Assess this cell for malaria.
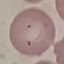
Parasitized.

stain: Giemsa
image_type: automatically extracted cell patch, resized to 64 × 64 pixels
preparation: thin smear
capture: smartphone through the microscope eyepiece